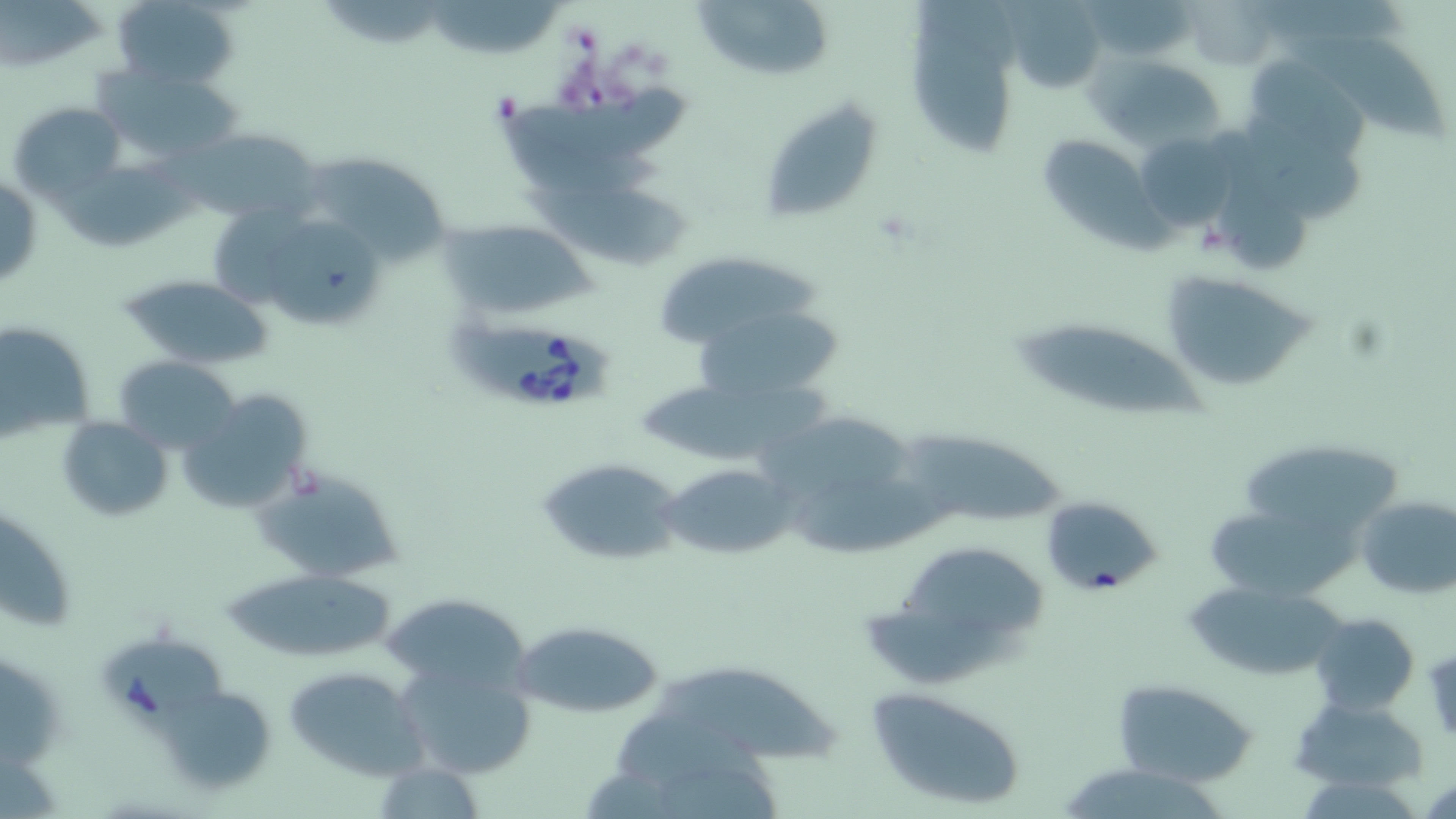 Approximate bounding boxes as (x1,y1)-(x2,y2) corner pairs in pixels. Babesia divergens-infected red blood cell locations: (448,322)-(617,409), (101,640)-(229,732). Uninfected red blood cell locations: (112,0)-(240,90), (1181,0)-(1279,70), (0,1)-(106,72), (429,1)-(567,57), (691,1)-(834,79), (1001,2)-(1109,91), (910,27)-(1013,159), (1296,35)-(1448,151), (1094,56)-(1224,150), (1256,59)-(1379,168), (95,64)-(248,172), (759,97)-(886,227), (10,102)-(124,204), (1243,118)-(1365,221), (182,126)-(322,225), (1137,131)-(1235,229), (1040,137)-(1173,254), (308,154)-(453,262), (0,174)-(42,291), (522,190)-(696,270), (445,219)-(593,318), (266,221)-(389,321), (661,257)-(825,340), (1158,268)-(1321,394), (118,274)-(275,371), (699,313)-(851,400), (0,321)-(96,443), (1017,322)-(1215,422), (115,356)-(240,453), (639,380)-(831,460), (179,389)-(312,515), (57,416)-(171,521), (759,416)-(922,502), (902,426)-(1073,523), (1247,444)-(1392,530), (535,457)-(683,567), (661,463)-(794,562), (256,469)-(407,584), (790,482)-(956,555), (1356,494)-(1455,598), (1039,495)-(1163,597), (1211,508)-(1361,602), (0,512)-(78,633), (898,549)-(1048,627), (224,569)-(397,662), (1187,583)-(1353,675), (377,592)-(536,689), (866,605)-(1033,687), (1309,613)-(1420,714), (512,617)-(667,719), (395,660)-(535,782), (282,666)-(426,781), (660,672)-(845,763), (1114,679)-(1258,785), (865,684)-(1030,812), (155,685)-(279,797), (1292,695)-(1429,795), (1063,770)-(1220,819). Slide-level diagnosis: Babesia divergens. May-Grünwald-Giemsa stain. Single field of view. Image is 1456×819 pixels. Optical microscopy. Thin blood film. 1000x magnification.